Point out each Plasmodium parasite.
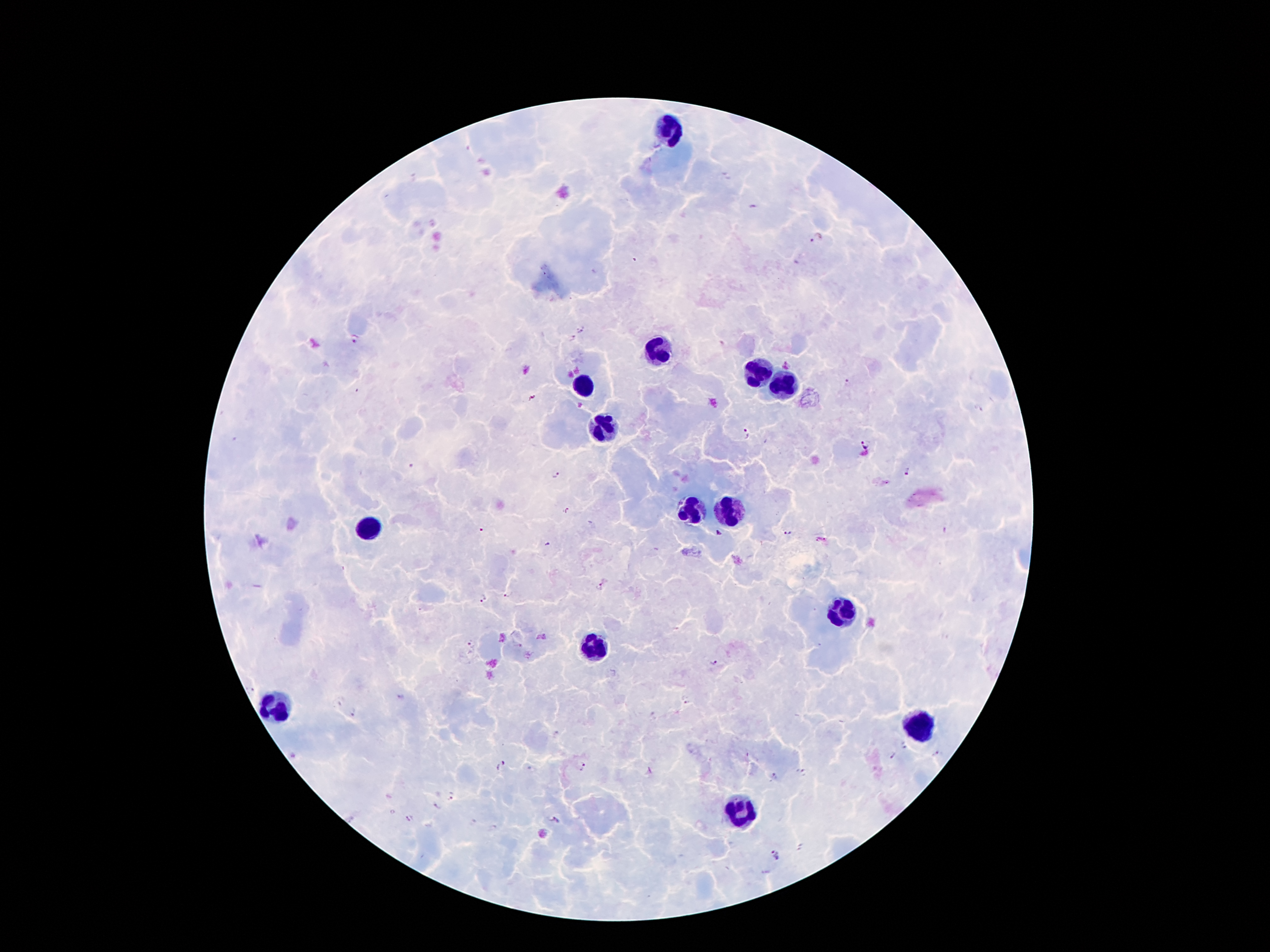
Approximate object centers, in pixels from the top-left corner.
Plasmodium parasites: (x=816, y=238), (x=356, y=339), (x=788, y=365), (x=847, y=383), (x=747, y=435), (x=864, y=444), (x=906, y=472), (x=556, y=475), (x=567, y=510), (x=787, y=532), (x=718, y=534), (x=599, y=587), (x=507, y=595), (x=483, y=597), (x=473, y=643), (x=714, y=662), (x=354, y=713), (x=936, y=754), (x=892, y=756), (x=502, y=765), (x=582, y=765), (x=803, y=773), (x=775, y=776), (x=450, y=798), (x=412, y=818), (x=555, y=820), (x=778, y=855).

{
  "leukocyte_locations": "approximate object centers, in pixels from the top-left corner: (x=669, y=130), (x=658, y=350), (x=756, y=371), (x=788, y=385), (x=581, y=387), (x=604, y=433), (x=691, y=510), (x=723, y=513), (x=371, y=527), (x=835, y=609), (x=597, y=650), (x=275, y=714), (x=914, y=725), (x=739, y=814)",
  "field_of_view": "single",
  "magnification": "100x",
  "capture": "smartphone through the microscope eyepiece",
  "preparation": "thick blood film",
  "image_size": "1270×952 pixels",
  "stain": "Giemsa",
  "patient_malaria_status": "positive for Plasmodium falciparum"
}